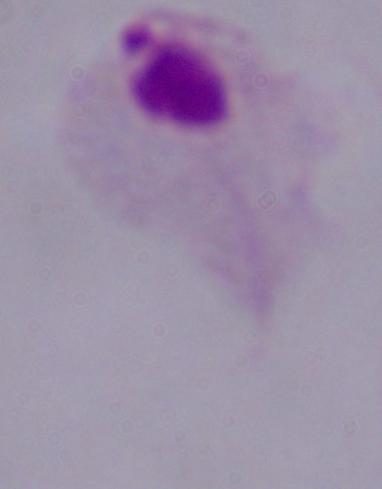
{
  "magnification": "1000x",
  "modality": "photomicrograph",
  "identification": "trichomonad"
}